State the preparation type.
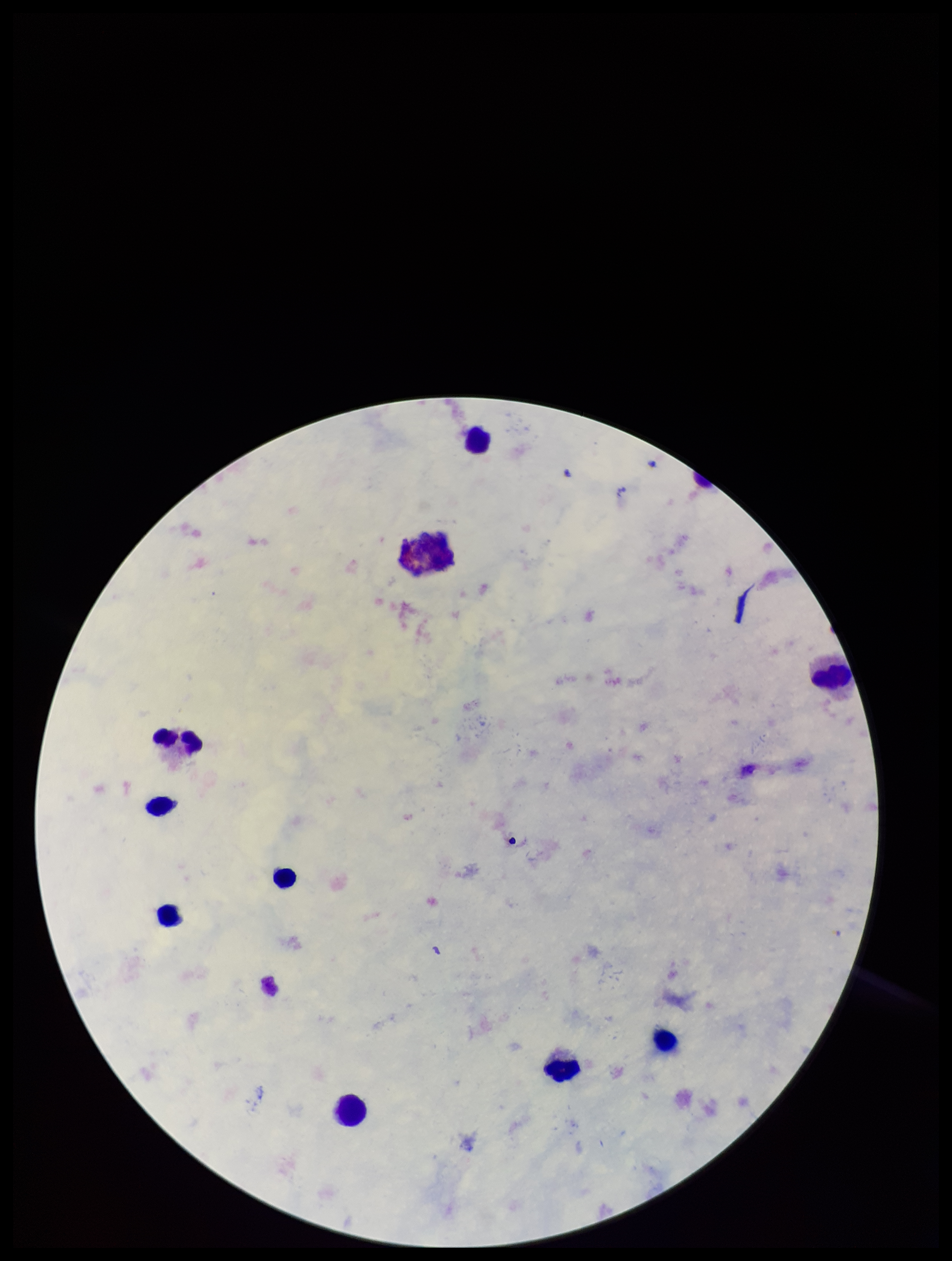
A thick smear.

image_size: 952×1261 pixels
stain: Giemsa
capture: smartphone photograph through the microscope eyepiece
leukocyte_count: 10
species_reported_for_this_patient: Plasmodium falciparum
patient_malaria_status: positive
parasite_count: 0
plasmodium_parasites: none detected
field_of_view: one from this slide